Give the extent of all Plasmodium malariae-infected red blood cells.
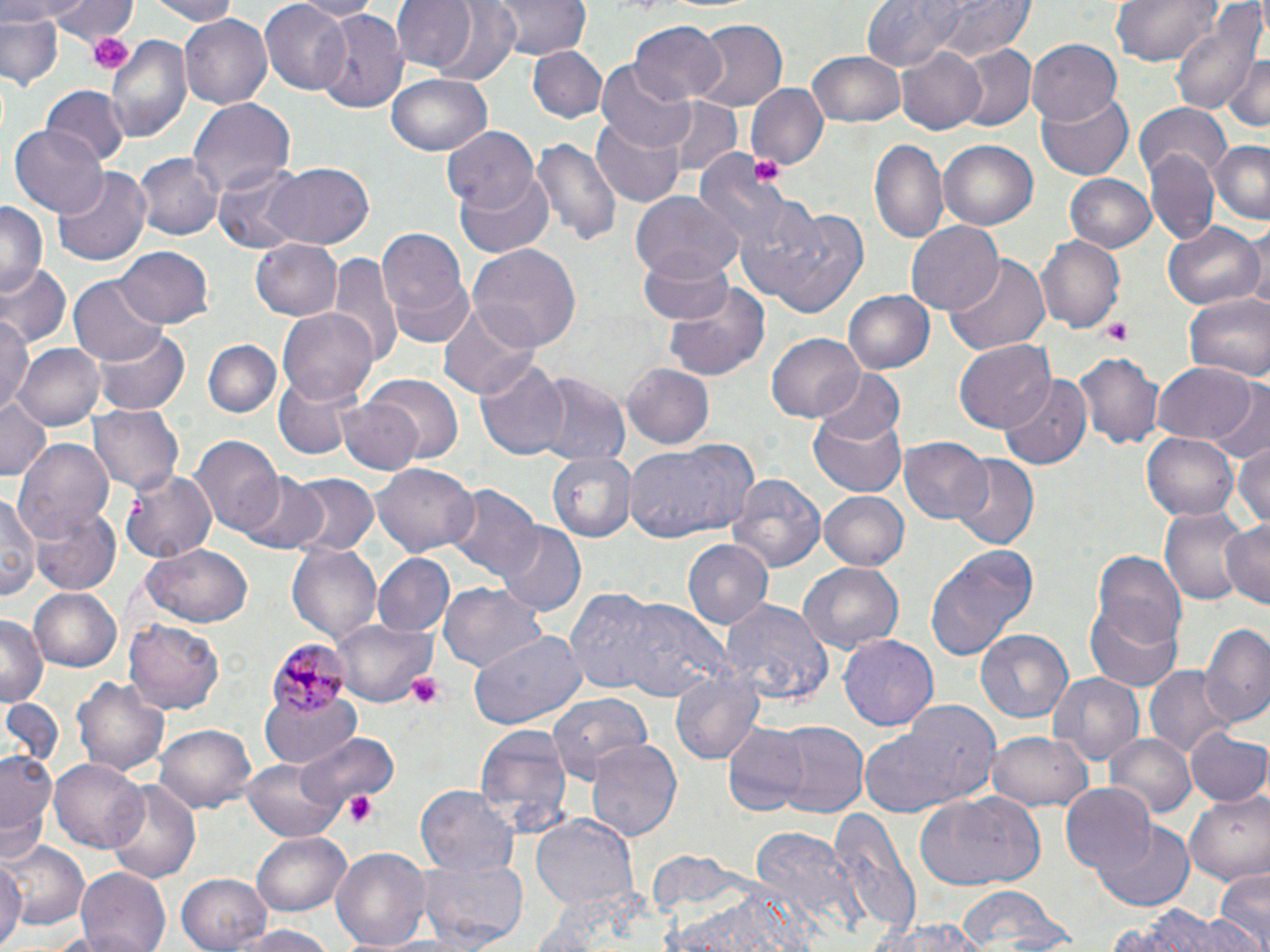
Approximate bounding boxes as (x1, y1, x2, y2) in pixels.
Plasmodium malariae-infected red blood cells: (264, 638, 351, 720).

Summary:
  - Uninfected red blood cell locations: (0, 0, 82, 23), (50, 0, 137, 43), (140, 0, 242, 24), (293, 0, 377, 20), (389, 0, 483, 75), (417, 0, 526, 86), (492, 0, 591, 60), (937, 0, 1033, 59), (1109, 0, 1224, 67), (261, 1, 352, 94), (859, 1, 968, 71), (1168, 6, 1266, 118), (311, 8, 410, 116), (0, 10, 66, 91), (181, 14, 272, 108), (689, 17, 788, 109), (629, 21, 725, 105), (105, 32, 192, 143), (1026, 37, 1123, 125), (954, 45, 1035, 133), (529, 46, 606, 122), (896, 46, 988, 136), (807, 49, 908, 127), (1225, 50, 1268, 135), (599, 60, 695, 152), (387, 73, 492, 157), (746, 83, 828, 170), (41, 85, 130, 167), (1037, 89, 1132, 180), (658, 96, 743, 174), (187, 97, 294, 201), (1135, 103, 1229, 181), (591, 116, 687, 207), (9, 124, 107, 218), (444, 127, 539, 214), (531, 134, 622, 250), (868, 137, 947, 246), (1209, 138, 1269, 224), (940, 140, 1037, 230), (695, 150, 791, 249), (1147, 151, 1218, 247), (137, 154, 221, 242), (263, 162, 376, 249), (213, 166, 310, 252), (53, 168, 151, 269), (454, 171, 555, 258), (1064, 172, 1160, 253), (630, 192, 744, 283), (0, 202, 44, 298), (761, 206, 872, 318), (905, 220, 1003, 315), (1161, 222, 1263, 310), (374, 226, 472, 343), (1242, 226, 1269, 312), (1035, 235, 1126, 334), (251, 238, 342, 320), (468, 244, 582, 351), (113, 245, 215, 327), (328, 251, 400, 364), (640, 254, 737, 324), (944, 255, 1050, 358), (2, 265, 71, 347), (70, 276, 164, 366), (662, 285, 771, 381), (844, 289, 935, 373), (1182, 292, 1270, 384), (437, 303, 538, 399), (279, 308, 379, 406), (0, 315, 34, 412), (94, 326, 191, 415), (767, 333, 864, 422), (203, 339, 282, 419), (956, 340, 1057, 431), (14, 343, 105, 432), (1072, 352, 1165, 450), (476, 357, 571, 462), (1152, 361, 1257, 444), (623, 363, 715, 448), (814, 368, 906, 445), (532, 372, 629, 467), (999, 374, 1094, 468), (274, 375, 362, 460), (361, 375, 465, 462), (1209, 381, 1270, 463), (0, 395, 52, 480), (338, 398, 423, 475), (809, 404, 911, 498), (88, 406, 184, 494), (1142, 432, 1241, 523), (194, 436, 284, 536), (13, 437, 113, 541), (898, 437, 993, 526), (624, 439, 760, 544), (1232, 439, 1270, 535), (551, 451, 636, 541), (948, 456, 1039, 549), (376, 463, 479, 556), (119, 470, 216, 565), (239, 473, 331, 553), (285, 473, 378, 557), (728, 476, 824, 572), (444, 484, 540, 581), (2, 489, 41, 605), (819, 490, 909, 569), (0, 497, 81, 601), (31, 506, 120, 595), (1157, 506, 1250, 605), (1219, 519, 1269, 612), (496, 523, 585, 616), (682, 540, 771, 631), (288, 541, 384, 644), (140, 545, 254, 626), (926, 545, 1035, 659), (1092, 549, 1186, 647), (374, 554, 455, 638), (798, 563, 904, 657), (440, 584, 546, 673), (28, 587, 120, 671), (566, 587, 667, 694), (1086, 598, 1183, 693), (621, 599, 729, 702), (722, 600, 832, 708), (0, 614, 44, 706), (335, 617, 436, 709), (125, 620, 225, 713), (1201, 621, 1270, 730), (974, 630, 1073, 727), (468, 632, 587, 729), (839, 636, 937, 730), (1146, 664, 1235, 759), (670, 668, 763, 763), (72, 672, 170, 777), (1047, 672, 1146, 769), (262, 689, 360, 766), (547, 692, 651, 783), (0, 697, 63, 771), (860, 706, 999, 817), (771, 721, 868, 819), (156, 724, 257, 814), (474, 725, 571, 834), (724, 727, 806, 815), (1186, 727, 1270, 807), (986, 731, 1091, 813), (303, 732, 399, 811), (1106, 733, 1196, 819), (584, 739, 683, 843), (2, 748, 59, 858), (243, 757, 348, 842), (52, 759, 148, 854), (105, 778, 202, 884), (417, 785, 520, 879), (1058, 785, 1157, 879), (1184, 791, 1270, 886), (916, 793, 1044, 892), (828, 811, 920, 938), (531, 814, 638, 917), (1098, 820, 1194, 907), (746, 826, 861, 934), (252, 833, 352, 916), (2, 838, 86, 927), (331, 845, 434, 952), (0, 854, 24, 949), (414, 855, 529, 948), (74, 868, 171, 951), (1213, 869, 1270, 952), (177, 871, 274, 951), (956, 887, 1060, 951), (659, 893, 817, 952), (1110, 905, 1257, 952), (870, 917, 985, 952), (223, 925, 338, 952)
  - Platelet locations: (88, 30, 134, 75), (749, 157, 781, 185), (1099, 320, 1133, 344), (405, 671, 448, 712), (344, 792, 380, 827)
  - Slide-level diagnosis: Plasmodium malariae
  - Magnification: 1000x
  - Modality: light microscopy
  - Image size: 1270×952 pixels
  - Preparation: thin blood film
  - Field of view: single
  - Stain: May-Grünwald-Giemsa